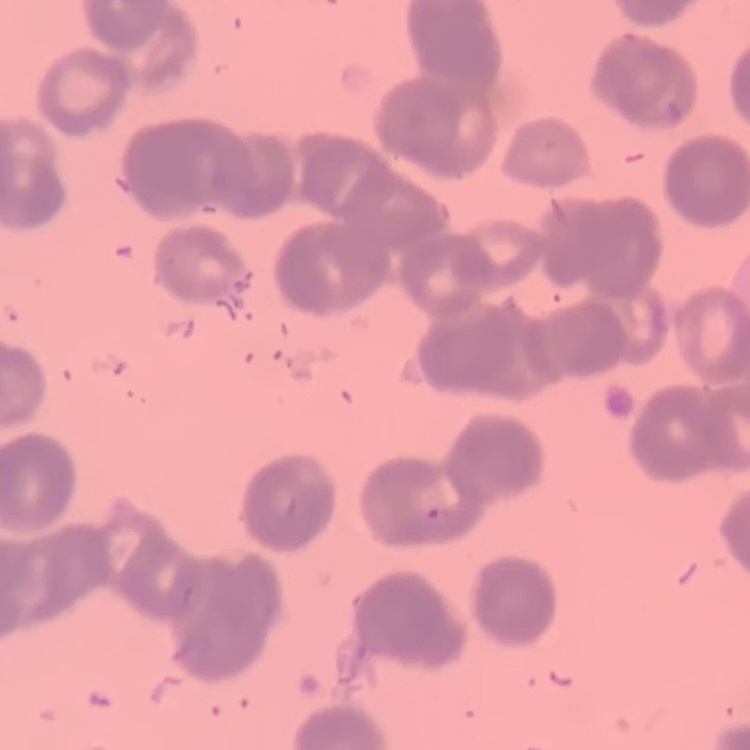 The erythrocytes exhibit rouleaux formation. Square crop of a larger photomicrograph. Stained with either Field's or Giemsa. Thin blood smear.